Assess for parasitized red blood cells.
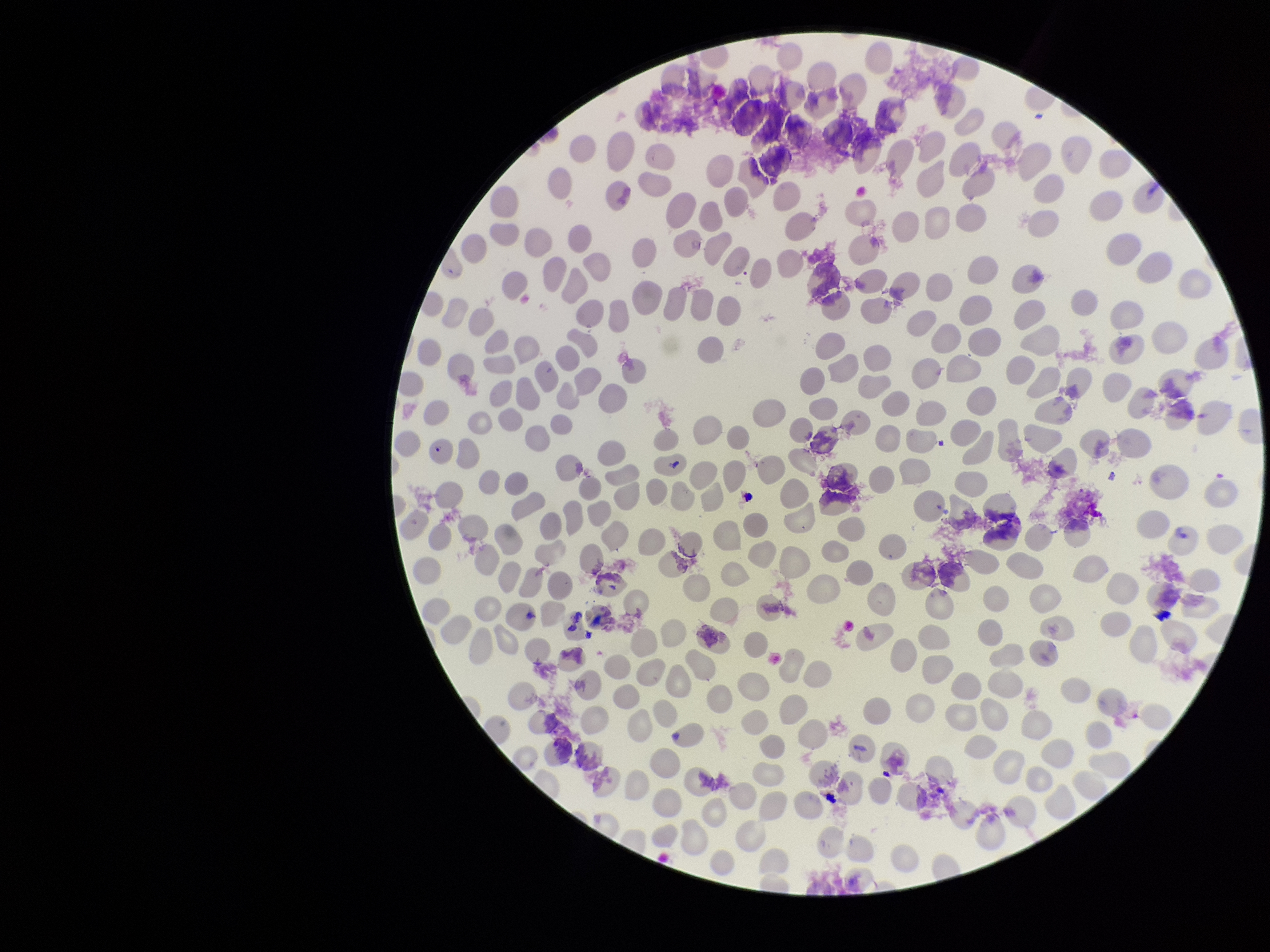

None identified.

Summary:
  - Capture: smartphone photograph through the microscope eyepiece
  - Image size: 1270×952 pixels
  - Red blood cell count: 287
  - Field of view: one from this slide
  - Patient malaria status: positive
  - Stain: Giemsa
  - Parasitized red blood cell count: 0
  - Species reported for this patient: Plasmodium falciparum
  - Preparation: thin smear